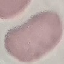

malaria status = uninfected
capture = smartphone camera at the microscope eyepiece
image type = automatically extracted cell patch, resized to 64 × 64 pixels
stain = Giemsa
preparation = thin smear